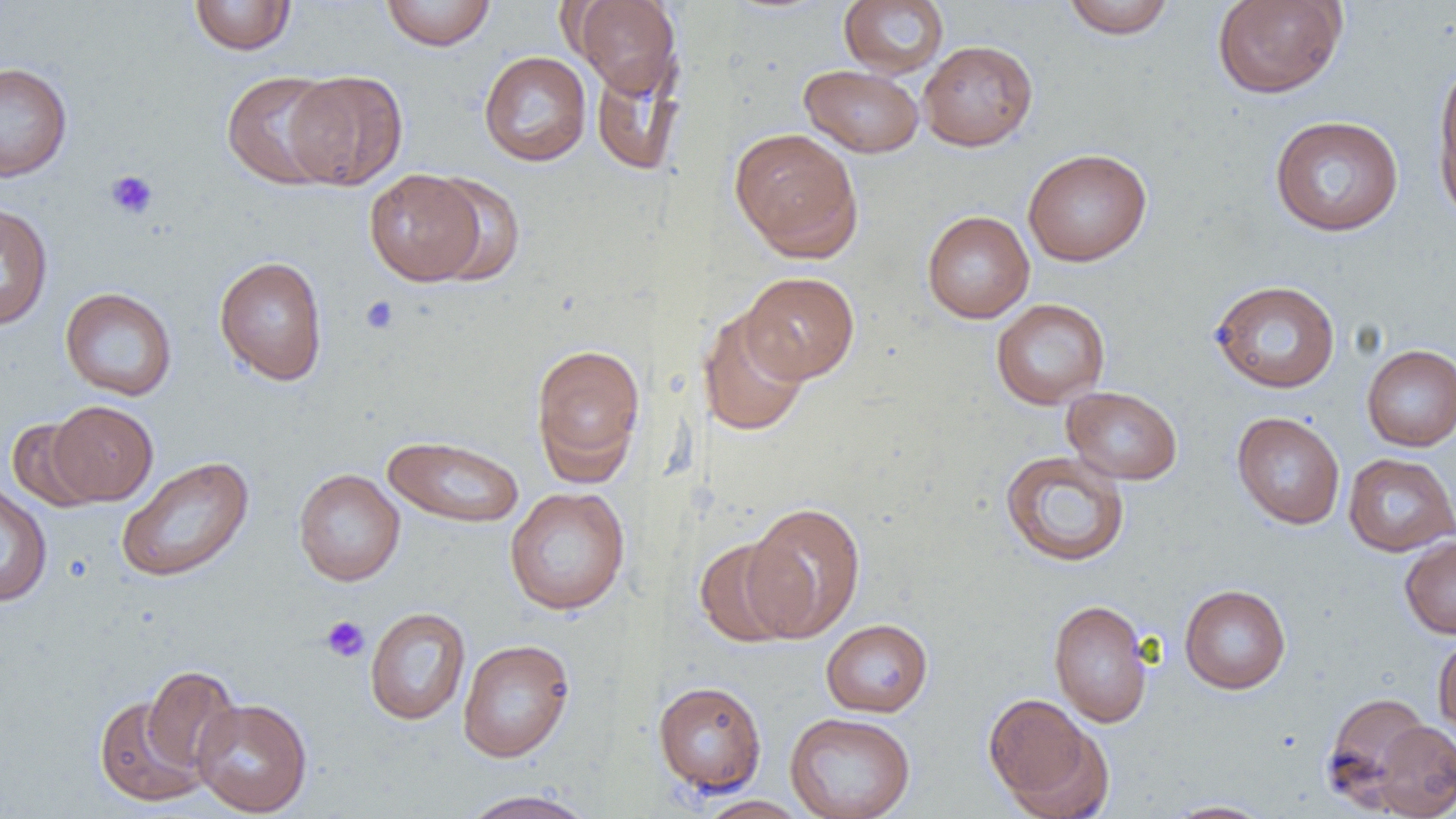 Approximate bounding boxes as (x1,y1)-(x2,y2) corner pairs in pixels. Uninfected red blood cell locations: (188,0)-(298,55), (380,0)-(497,51), (839,0)-(949,78), (1060,0)-(1176,39), (1211,0)-(1347,99), (571,1)-(681,97), (918,40)-(1038,151), (478,51)-(592,167), (591,58)-(685,176), (1433,58)-(1456,223), (0,61)-(73,182), (799,64)-(924,158), (221,70)-(344,190), (284,71)-(408,190), (1269,115)-(1404,236), (728,127)-(863,259), (1023,148)-(1152,266), (364,168)-(487,285), (425,174)-(525,286), (0,201)-(53,331), (921,210)-(1035,323), (213,256)-(328,385), (740,271)-(860,382), (1209,279)-(1341,393), (60,287)-(177,401), (991,298)-(1110,409), (697,308)-(812,437), (530,342)-(646,481), (1361,344)-(1456,451), (1062,386)-(1183,485), (47,400)-(159,505), (1231,411)-(1345,530), (6,417)-(105,512), (382,433)-(525,528), (999,450)-(1130,567), (1342,453)-(1456,557), (116,455)-(255,583), (293,468)-(406,586), (0,482)-(53,607), (504,486)-(631,615), (742,501)-(867,642), (1399,535)-(1456,638), (692,537)-(807,648), (1179,584)-(1291,694), (1048,599)-(1154,727), (365,606)-(471,726), (820,618)-(933,717), (1433,634)-(1456,741), (457,638)-(575,762), (141,664)-(243,778), (652,680)-(767,797), (1322,691)-(1434,808), (984,693)-(1103,811), (94,694)-(207,807), (192,697)-(312,816), (784,712)-(916,819), (1370,720)-(1456,818), (457,789)-(598,819), (693,795)-(812,819), (1161,799)-(1276,818). Platelet locations: (105,170)-(159,220), (360,295)-(400,335), (320,615)-(370,663). Slide-level diagnosis: no evidence of blood parasites. Thin blood film. One field of a larger specimen. Captured at 1000x magnification. Image is 1456×819 pixels. Light microscopy.